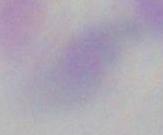

identification: Toxoplasma gondii
magnification: 1000x
modality: micrograph